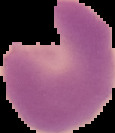
Cell region segmented out of the field of view; the surrounding area is masked to black. Malaria status: parasitized. Image is 115×133 pixels. From a thin blood film.